State the blood parasite species.
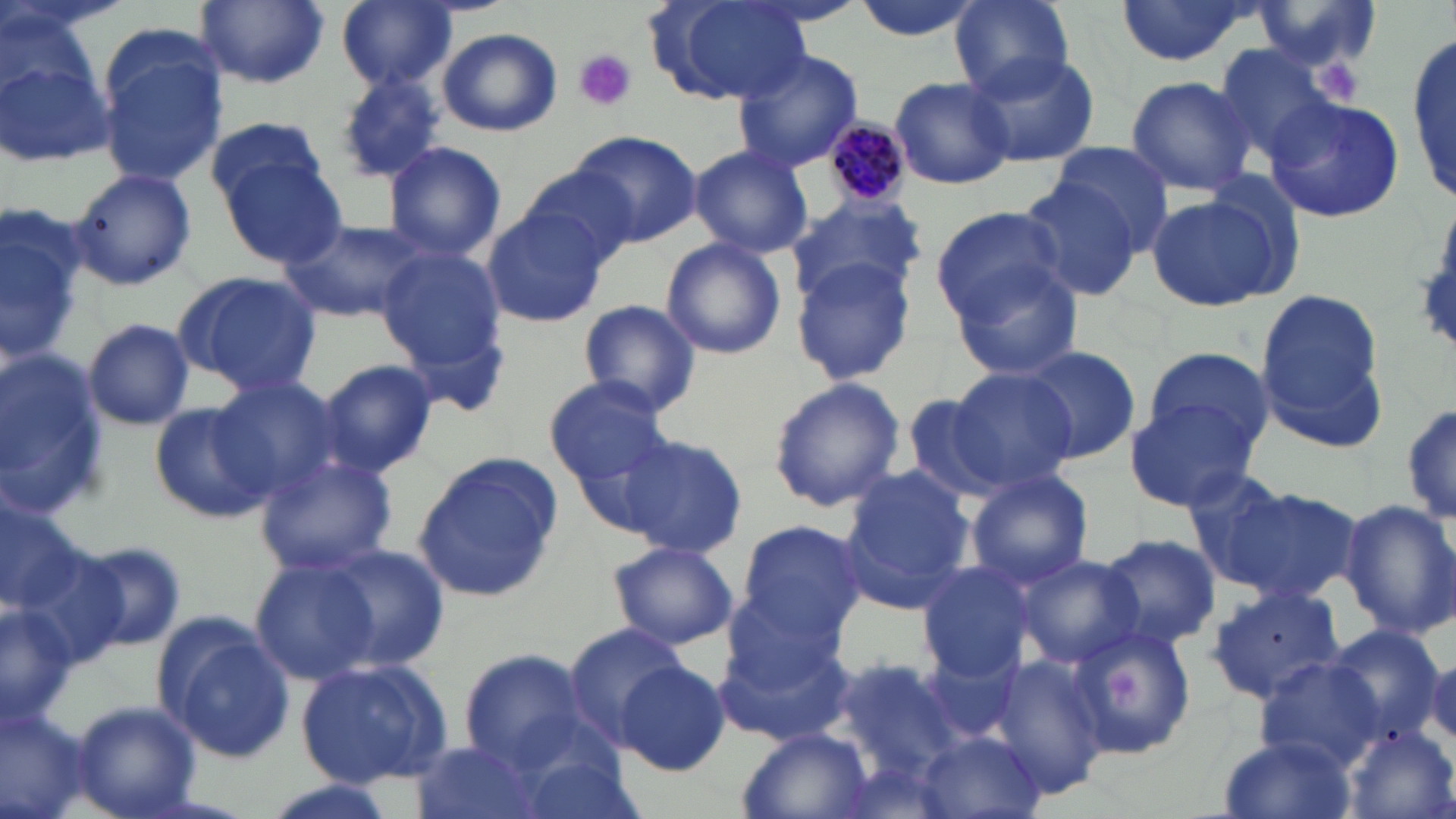
Plasmodium malariae.

Approximate bounding boxes as (x1, y1, x2, y2) in pixels. Plasmodium malariae-infected red blood cell locations: (823, 119, 911, 210). Uninfected red blood cell locations: (193, 0, 330, 87), (332, 0, 458, 93), (851, 0, 983, 42), (951, 0, 1074, 99), (1111, 0, 1258, 69), (647, 1, 810, 108), (1251, 1, 1387, 74), (0, 26, 116, 171), (96, 27, 229, 190), (438, 28, 562, 137), (1409, 34, 1454, 198), (1211, 43, 1344, 164), (733, 49, 865, 172), (959, 49, 1101, 168), (332, 72, 448, 185), (1125, 75, 1255, 196), (887, 76, 1014, 191), (1267, 95, 1404, 226), (205, 115, 329, 214), (569, 131, 701, 246), (384, 141, 506, 261), (1050, 141, 1173, 249), (690, 144, 813, 259), (219, 155, 345, 270), (518, 166, 640, 270), (70, 168, 196, 289), (1014, 174, 1144, 304), (1144, 189, 1289, 310), (787, 194, 926, 304), (1, 204, 91, 364), (481, 206, 608, 329), (931, 206, 1068, 324), (281, 218, 429, 325), (660, 237, 786, 360), (376, 247, 510, 374), (790, 256, 918, 386), (947, 260, 1086, 383), (173, 269, 322, 395), (1253, 287, 1388, 446), (578, 298, 702, 418), (82, 318, 194, 431), (1016, 344, 1140, 464), (1139, 346, 1278, 461), (0, 353, 108, 517), (319, 360, 440, 476), (939, 368, 1077, 495), (209, 376, 341, 504), (545, 378, 670, 486), (766, 378, 906, 514), (902, 390, 1030, 505), (1400, 394, 1455, 531), (1126, 397, 1263, 511), (148, 402, 274, 524), (615, 430, 748, 559), (254, 449, 400, 575), (412, 453, 561, 602), (837, 466, 979, 610), (1178, 466, 1304, 591), (964, 470, 1094, 590), (1208, 477, 1363, 606), (1339, 497, 1456, 642), (0, 502, 88, 616), (735, 518, 868, 643), (1093, 533, 1220, 650), (605, 539, 738, 651), (72, 541, 187, 654), (313, 542, 451, 674), (1016, 554, 1142, 670), (249, 555, 383, 684), (915, 560, 1037, 680), (725, 584, 851, 692), (1206, 584, 1348, 703), (0, 599, 74, 724), (714, 619, 856, 747), (157, 621, 296, 763), (565, 622, 692, 744), (1068, 623, 1196, 758), (1322, 625, 1446, 745), (917, 635, 1028, 745), (456, 650, 593, 770), (988, 650, 1111, 795), (1423, 650, 1456, 745), (296, 657, 452, 788), (832, 657, 973, 774), (1258, 658, 1384, 767), (613, 659, 731, 776), (69, 701, 199, 818), (0, 704, 96, 819), (1344, 725, 1453, 819), (740, 728, 872, 818), (914, 731, 1045, 816), (1220, 734, 1359, 819), (406, 739, 543, 819), (254, 775, 400, 819). Platelet locations: (574, 48, 637, 111), (1315, 51, 1369, 104), (1109, 668, 1141, 707). Thin blood smear. Image is 1456×819 pixels. 1000x magnification. May-Grünwald-Giemsa-stained preparation. Optical microscopy. One field of a larger specimen.